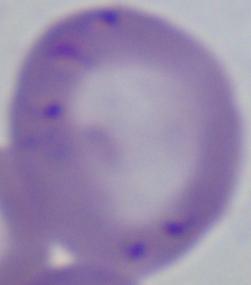
identification = Babesia
modality = micrograph
magnification = 1000x